Describe the morphology of the red blood cells.
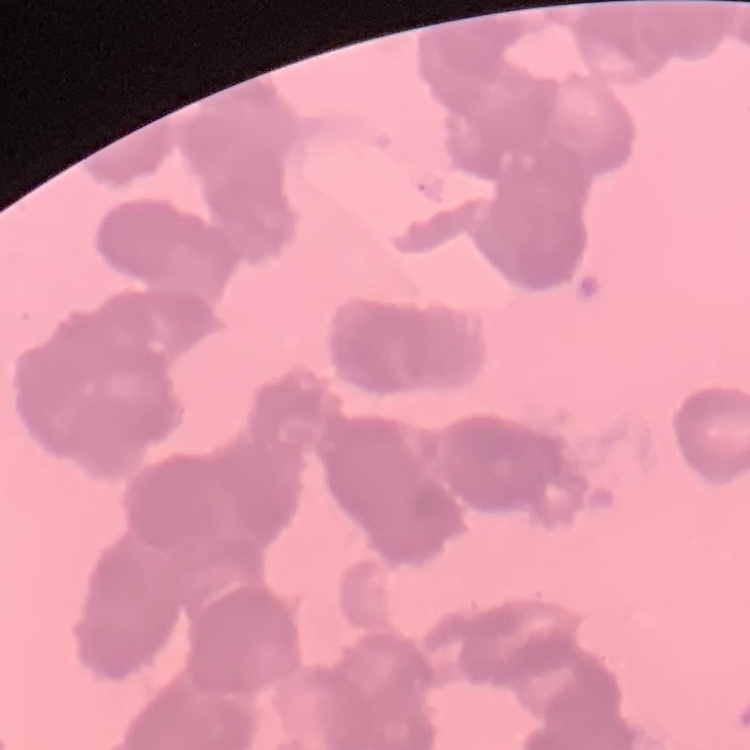

Rouleaux formation.

Summary:
  - Image type: square crop of a larger photomicrograph
  - Stain: Field's or Giemsa
  - Preparation: thin peripheral smear